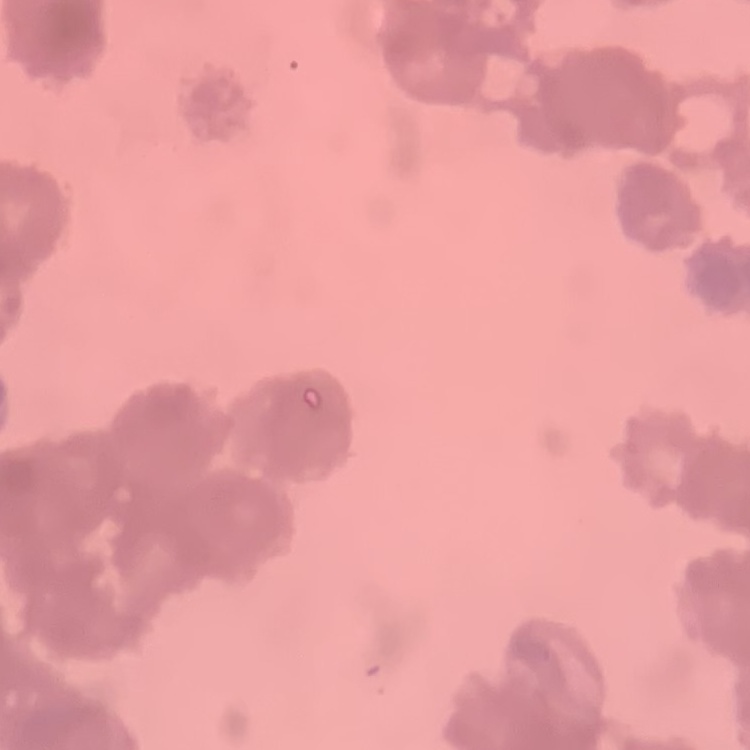 The red blood cells show rouleaux formation. One tile cut from a larger photomicrograph. Thin blood smear. Stained with either Field's or Giemsa.